State the preparation type.
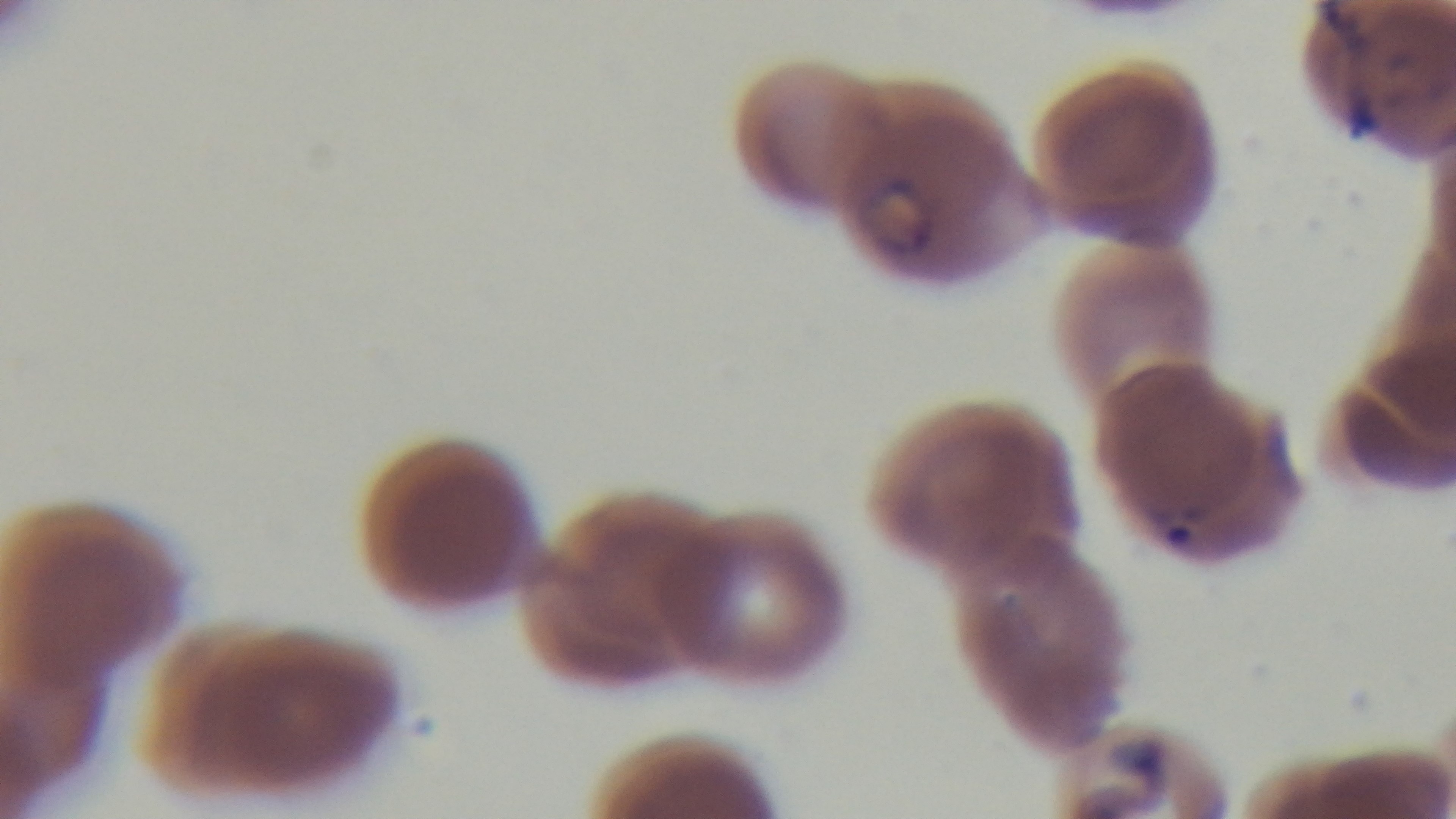
It is a thin blood film.

{
  "objective": "100x oil immersion",
  "malaria_status": "positive",
  "field_of_view": "one from the slide",
  "stain": "Giemsa",
  "modality": "light microscopy",
  "capture": "mounted 4K digital camera"
}